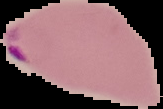

Result: Plasmodium parasites detected. From a thin blood smear. Image is 163×109 pixels. The area outside the segmented cell region is set to black.